Identify the preparation type.
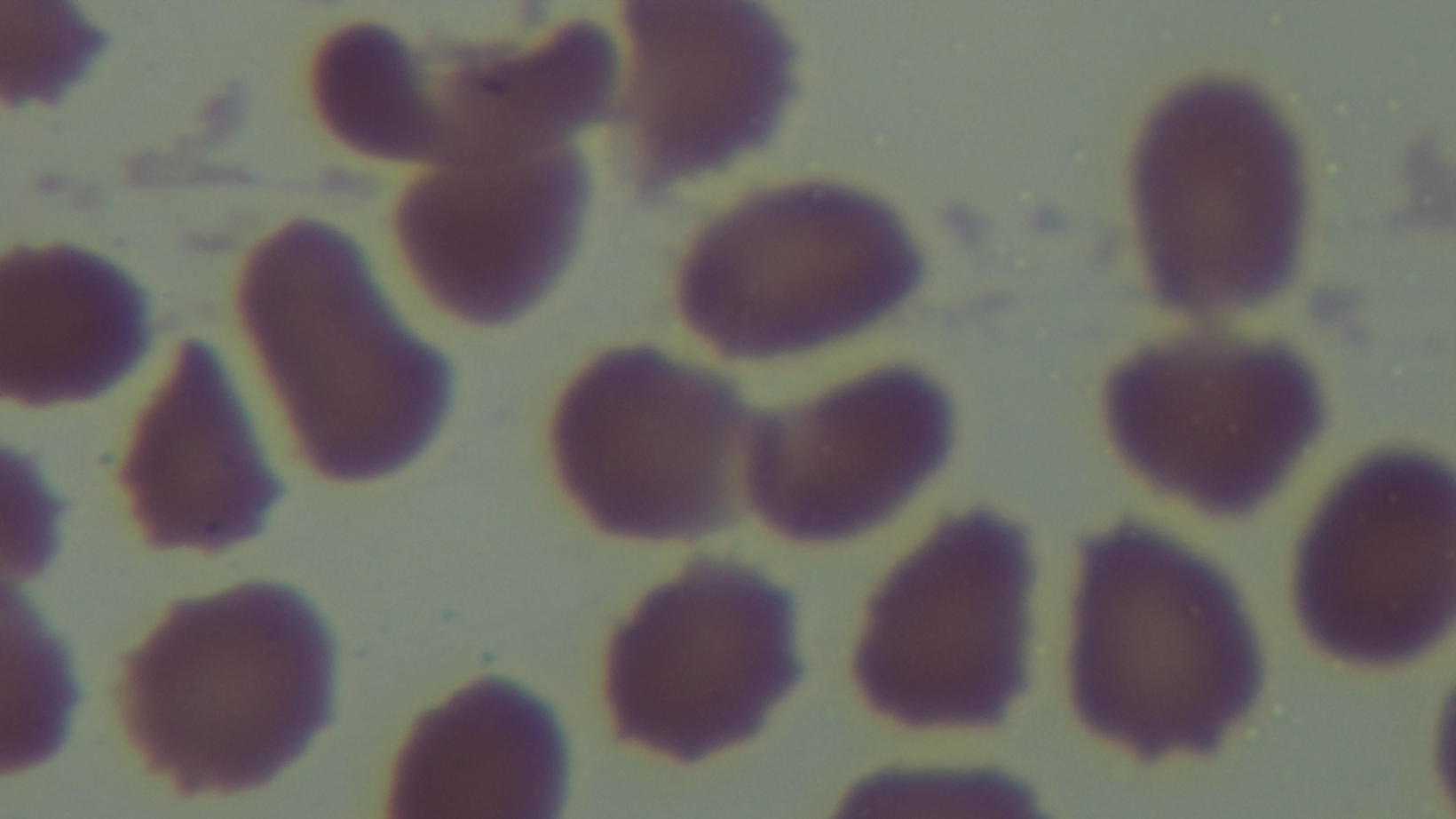
Thin.

Photomicrograph. One field from the slide. 100x oil-immersion objective. Captured with a mounted 4K digital camera. Malaria status: negative. Giemsa stain.